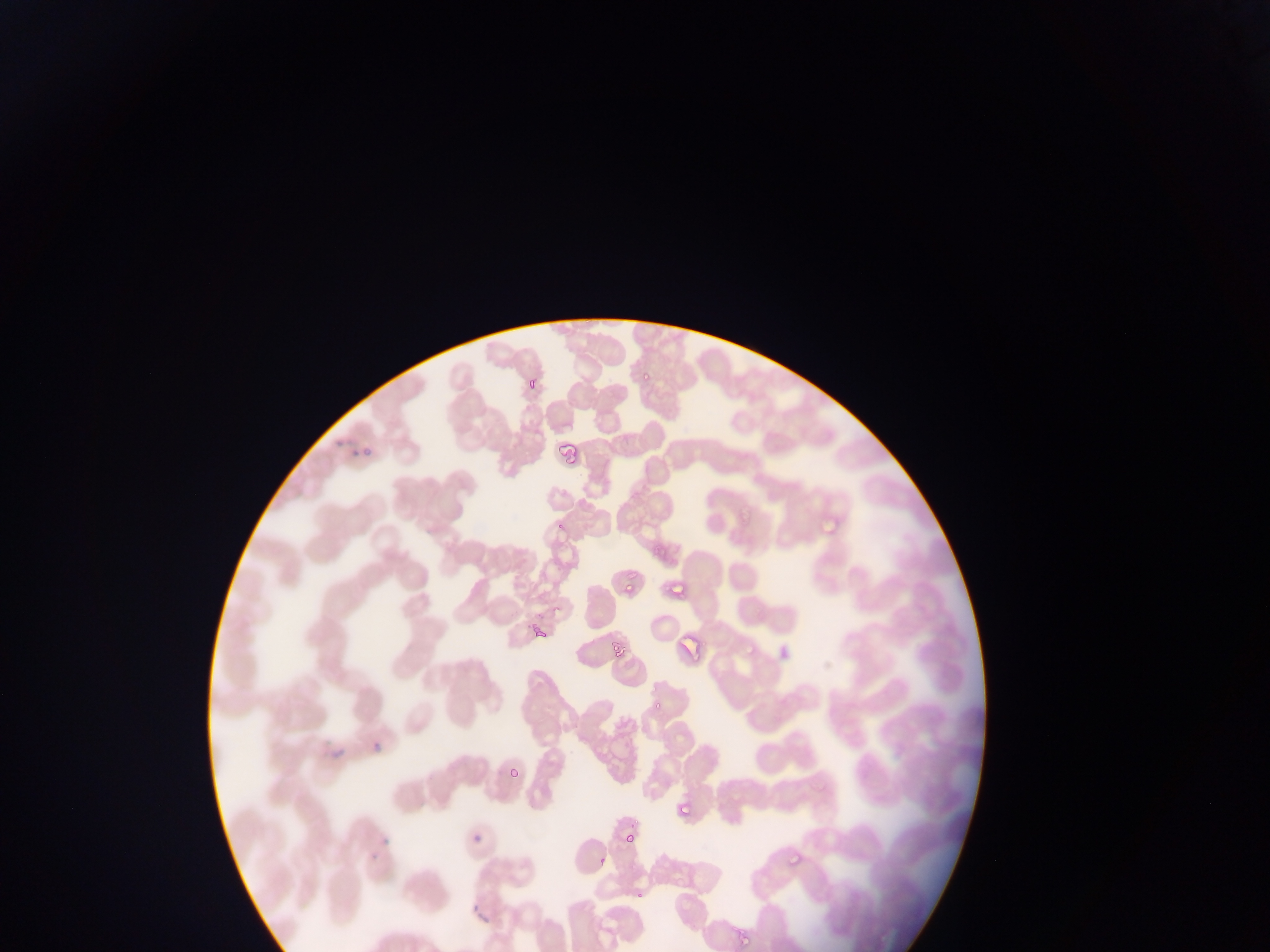
Plasmodium parasite locations = approximate bounding boxes as [left, top, right, bottom] in pixels: [636, 361, 654, 378], [519, 369, 552, 391], [550, 438, 583, 473], [812, 507, 842, 538], [734, 508, 765, 531], [618, 565, 651, 597], [662, 570, 687, 606], [528, 625, 553, 643], [608, 638, 631, 662], [370, 728, 391, 756], [320, 740, 347, 765], [501, 757, 526, 792], [662, 798, 700, 828], [380, 810, 403, 848], [619, 825, 635, 850], [469, 827, 484, 850], [365, 837, 382, 860], [773, 850, 815, 877], [596, 856, 609, 870], [323, 874, 339, 897], [628, 881, 653, 905], [730, 928, 755, 952]
image size = 1270×952 pixels
country = Ghana
field of view = single
capture = mobile-phone photograph through a microscope
preparation = thin blood film